Give the preparation type.
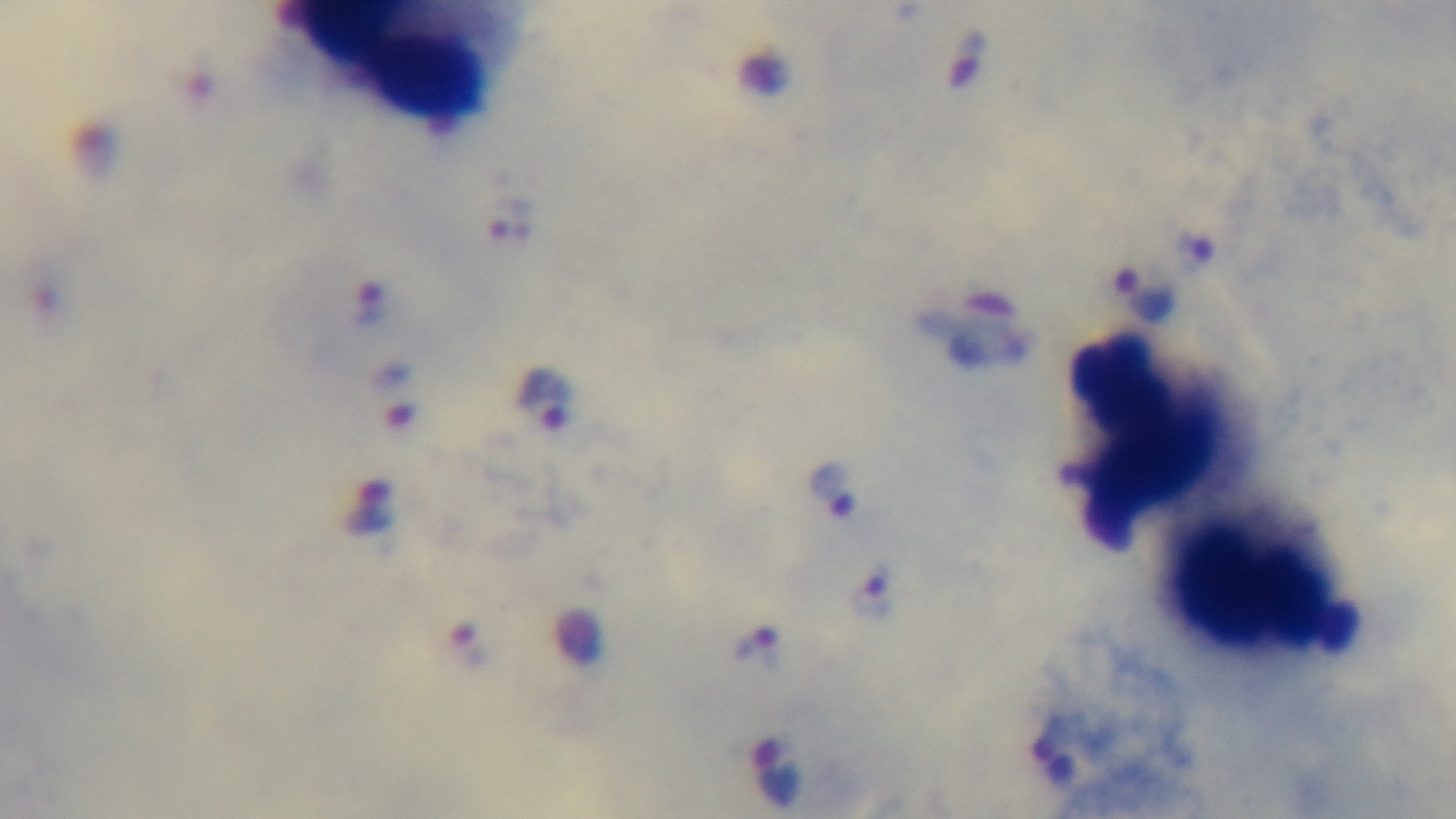

Thick.

{
  "stain": "Giemsa",
  "malaria_status": "infected",
  "modality": "light microscopy",
  "field_of_view": "one from the slide",
  "objective": "100x oil immersion",
  "capture": "mounted 4K digital camera"
}